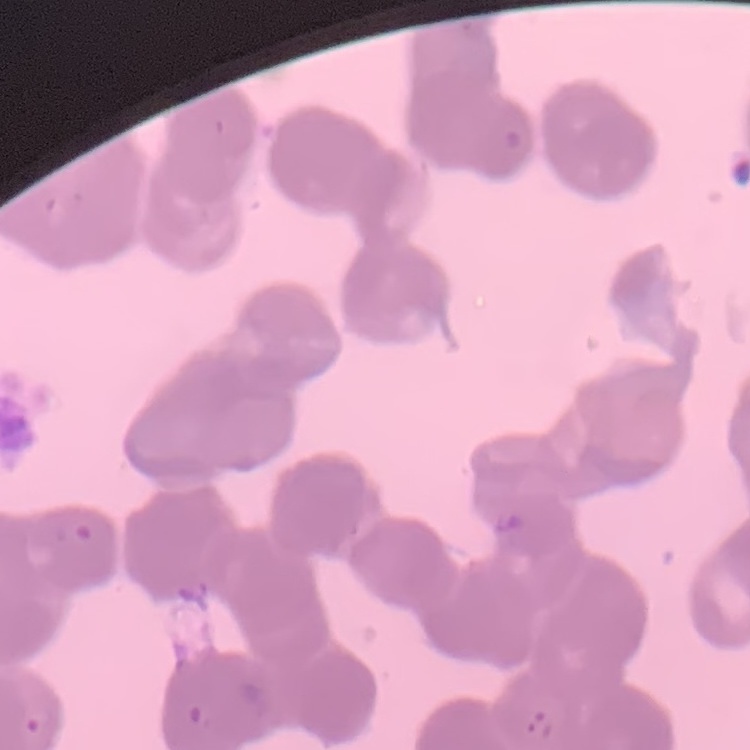
red blood cell morphology = rouleaux formation
image type = square crop of a larger photomicrograph
stain = Field's or Giemsa
preparation = thin peripheral smear